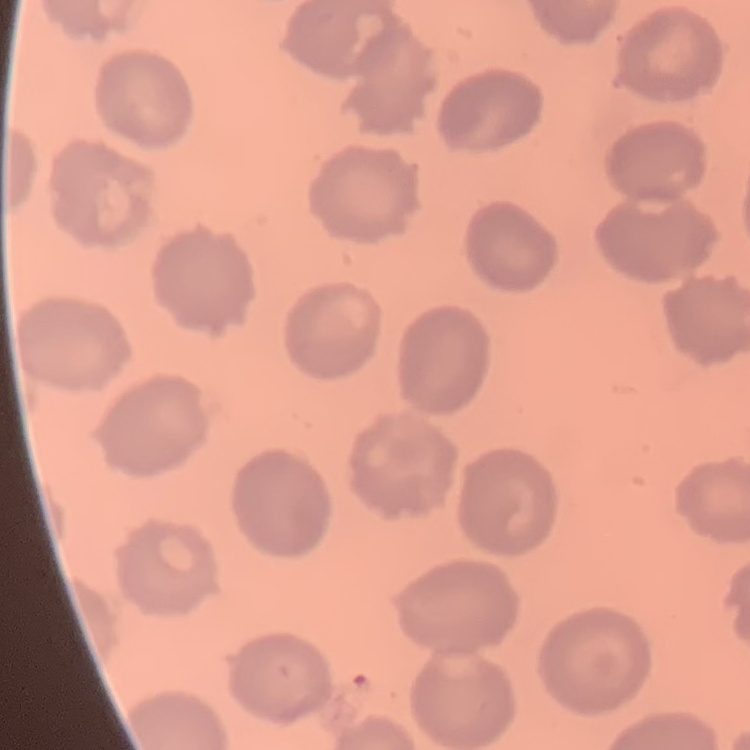
{
  "erythrocyte_morphology": "no rouleaux formation",
  "image_type": "square crop of a larger photomicrograph",
  "stain": "Field's or Giemsa",
  "preparation": "thin blood smear"
}